Locate platelets.
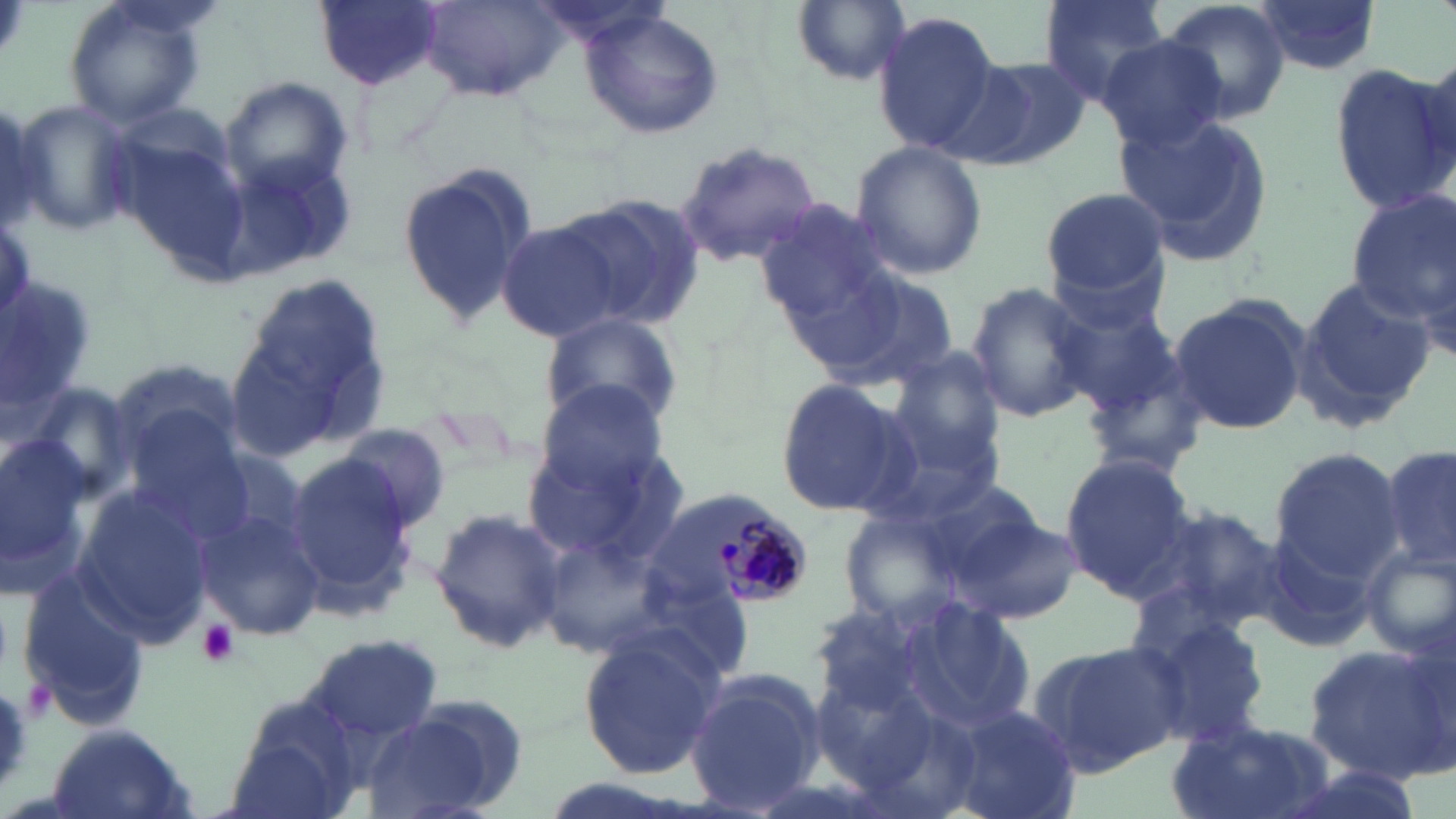
Approximate bounding boxes as (x1,y1)-(x2,y2) corner pairs in pixels.
Platelets: (197,620)-(238,668).

Plasmodium malariae-infected red blood cell locations: (709,511)-(808,606). Uninfected red blood cell locations: (1037,0)-(1173,105), (1159,0)-(1291,123), (63,1)-(210,130), (314,1)-(443,91), (790,1)-(911,87), (1251,1)-(1383,77), (417,2)-(568,104), (579,10)-(724,139), (873,11)-(1002,156), (1097,35)-(1230,150), (961,57)-(1096,171), (1331,64)-(1453,216), (218,76)-(352,197), (10,97)-(137,236), (0,102)-(57,238), (1113,109)-(1275,270), (848,140)-(989,284), (680,143)-(819,263), (225,147)-(358,278), (395,160)-(540,328), (1039,187)-(1173,308), (1345,190)-(1455,337), (567,193)-(706,328), (752,197)-(892,324), (494,219)-(636,345), (808,266)-(963,396), (225,274)-(392,460), (1290,275)-(1434,434), (964,280)-(1098,425), (1048,293)-(1183,413), (1167,296)-(1312,435), (539,309)-(687,435), (1076,342)-(1212,483), (105,357)-(250,481), (879,357)-(1009,501), (532,376)-(672,499), (771,378)-(908,517), (123,412)-(255,534), (335,423)-(451,533), (520,431)-(691,574), (0,437)-(94,583), (1380,441)-(1456,578), (1268,447)-(1403,584), (283,453)-(424,614), (1059,455)-(1199,598), (72,485)-(214,643), (1132,501)-(1289,637), (197,507)-(326,639), (429,508)-(567,655), (953,510)-(1084,626), (539,523)-(675,661), (1253,528)-(1385,656), (1359,544)-(1456,663), (16,566)-(152,730), (1133,606)-(1274,748), (577,629)-(723,782), (304,634)-(446,744), (1025,636)-(1186,776), (1304,642)-(1454,782), (685,667)-(826,814), (221,690)-(372,819), (367,701)-(522,819), (938,704)-(1080,819), (1167,721)-(1335,819), (41,722)-(201,819). Slide-level diagnosis: Plasmodium malariae. Single field of view. Thin blood smear. Image is 1456×819 pixels. Captured at 1000x magnification. Optical microscopy. May-Grünwald-Giemsa stain.